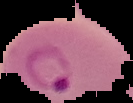
Summary:
  - Preparation: thin blood film
  - Malaria status: parasitized
  - Image size: 133×103 pixels
  - Image type: cell region segmented out of the field of view; surrounding area masked to black